Identify the parasite.
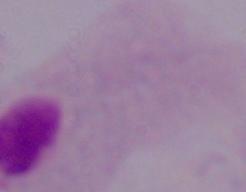

A trichomonad.

{
  "magnification": "1000x",
  "modality": "photomicrograph"
}